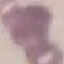

Summary:
  - Result: no malaria parasites detected
  - Image type: automatically extracted cell patch, resized to 64 × 64 pixels
  - Stain: Giemsa
  - Preparation: thin smear
  - Capture: smartphone camera at the microscope eyepiece